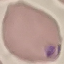

malaria status = parasitized
stain = Giemsa
capture = smartphone through the microscope eyepiece
image type = cell patch, automatically extracted from a larger field of view and resized to 64 × 64 pixels
preparation = thin blood film